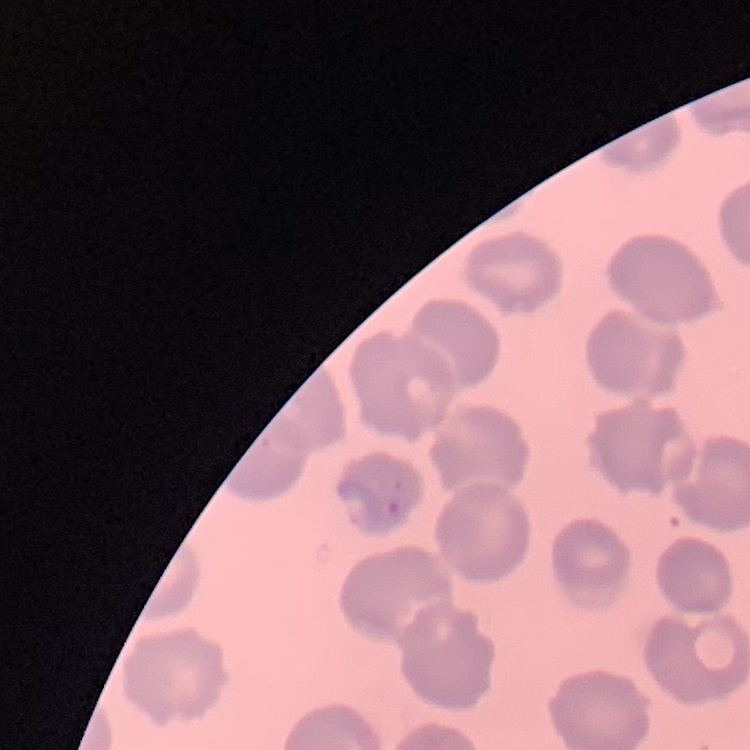
Summary:
  - Red blood cell morphology: no rouleaux formation
  - Stain: Field's or Giemsa
  - Preparation: thin blood smear
  - Image type: one tile cut from a larger photomicrograph